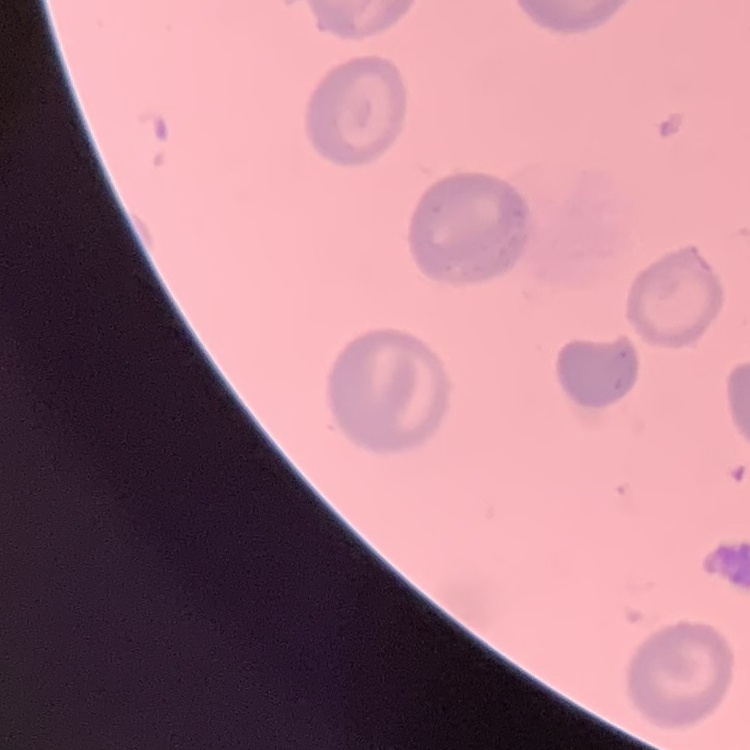 The red blood cells exhibit no rouleaux formation. Thin peripheral smear. One tile cut from a larger photomicrograph. Field's or Giemsa stain.